Classify this cell by malaria status.
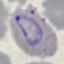

It is parasitized.

Summary:
  - Capture: smartphone camera at the microscope eyepiece
  - Stain: Giemsa
  - Preparation: thin smear
  - Image type: cell patch, automatically extracted from a larger field of view and resized to 64 × 64 pixels